Point out each leukocyte.
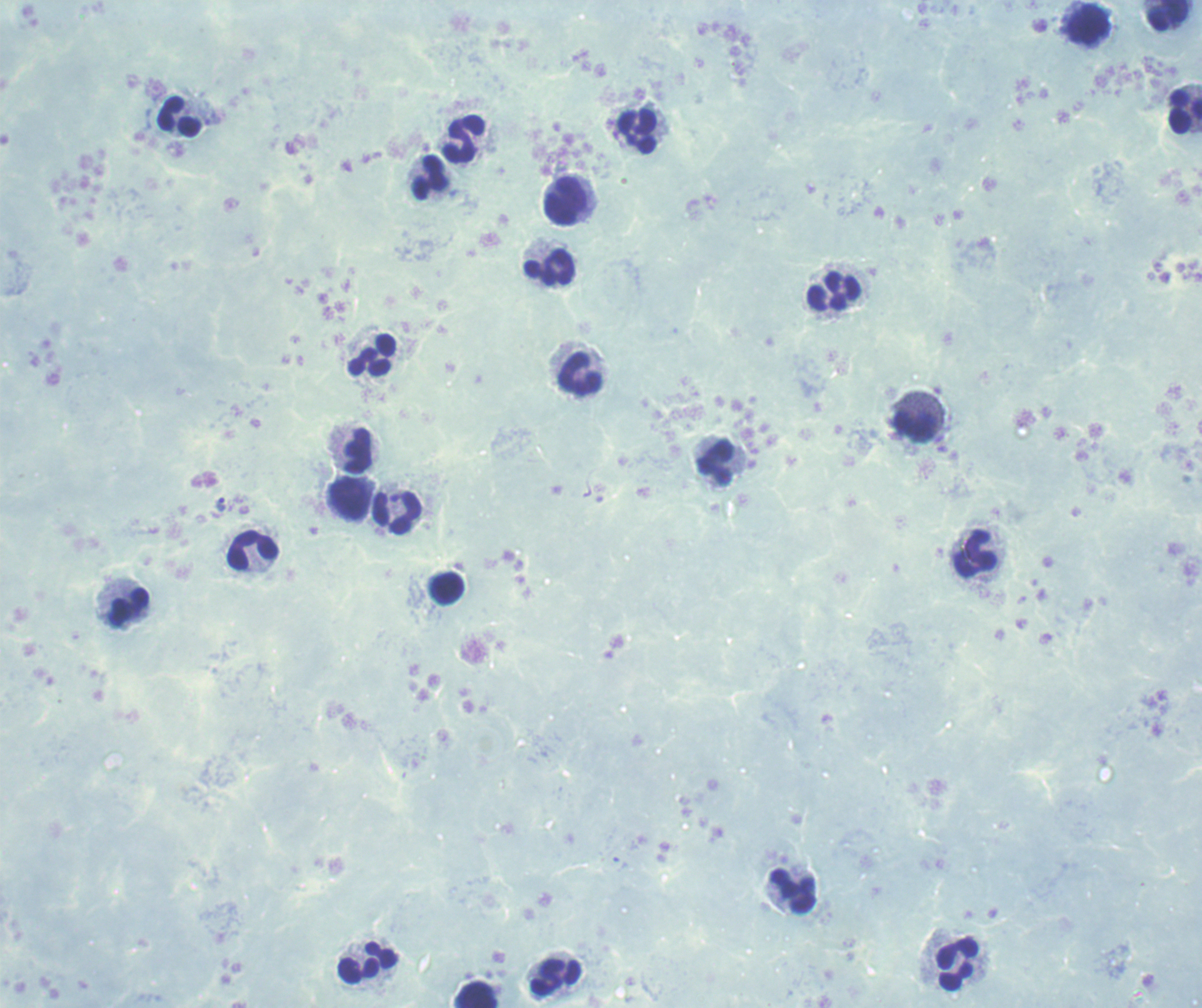
Approximate centers as (x, y) in pixels.
Leukocytes: (1168, 15), (1089, 25), (1185, 112), (180, 118), (638, 132), (464, 140), (430, 177), (567, 201), (550, 268), (834, 292), (373, 355), (581, 374), (915, 426), (358, 451), (716, 463), (350, 499), (398, 513), (253, 550), (976, 554), (447, 589), (130, 608), (794, 892), (367, 963), (958, 964), (555, 977), (474, 995).

Approximate centers as (x, y) in pixels.
Summary:
  - Trophozoite locations: (220, 503)
  - Field of view: one from this slide
  - Preparation: thick smear of blood
  - Magnification: 100x
  - Background quality: unsatisfactory
  - Result: malaria parasites detected
  - Image size: 1202×1008 pixels
  - Stain: Romanowsky
  - Context: previously used in an actual diagnosis